Give the extent of the malaria parasites you find, grouped by life-cycle stage — ring form, trophozoite, schizont, or gametocyte.
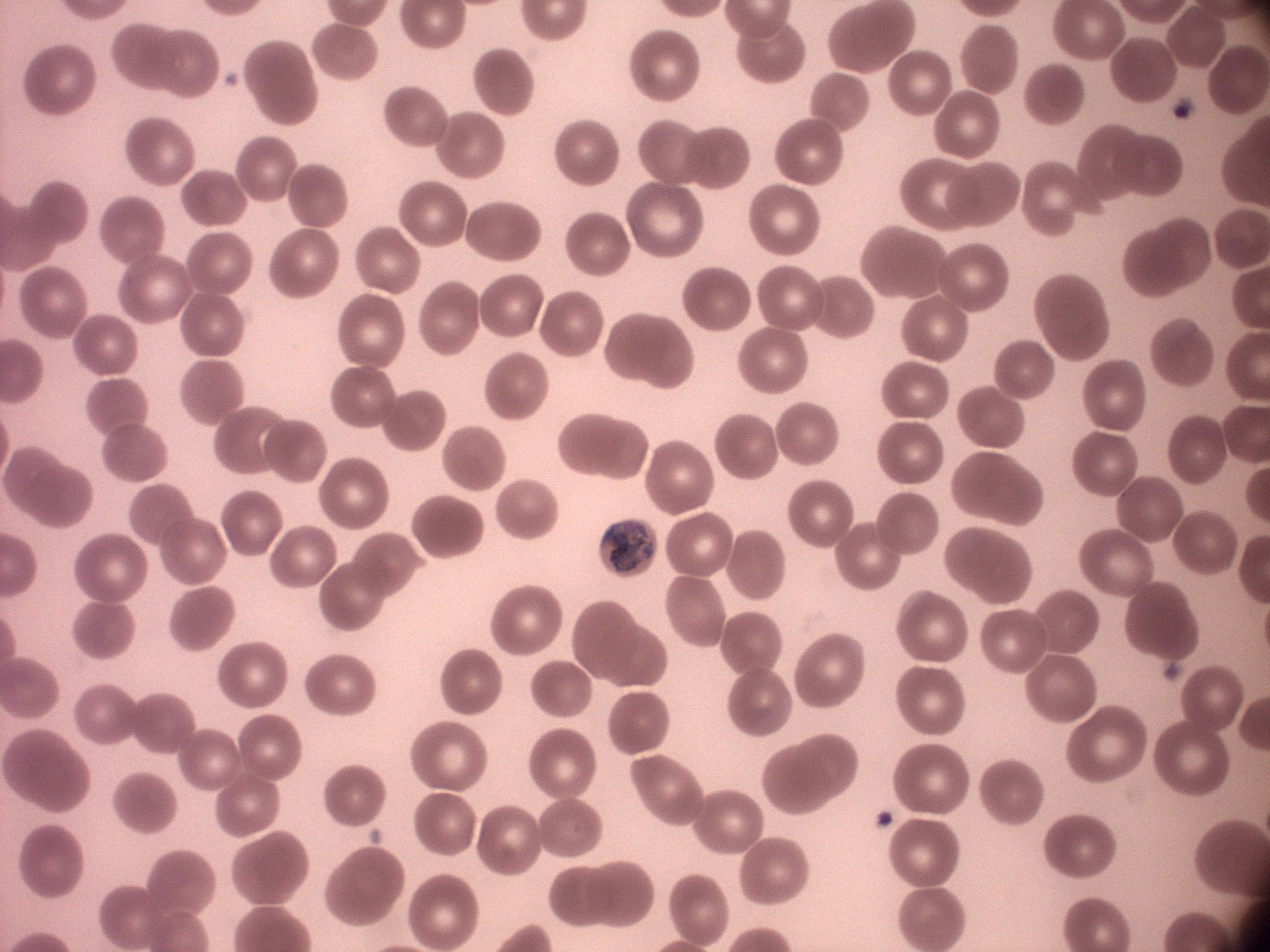
Approximate bounding boxes as named x1/y1/x2/y2 corners in pixels, from the source annotation, which is not necessarily exhaustive.
Trophozoites: (x1=608, y1=520, x2=658, y2=577).

species = Plasmodium malariae
field of view = one from this slide
microscope = Leica DM2000 with built-in camera
preparation = thin blood film
magnification = 100x
stain = Giemsa
image size = 1270×952 pixels